State the preparation type.
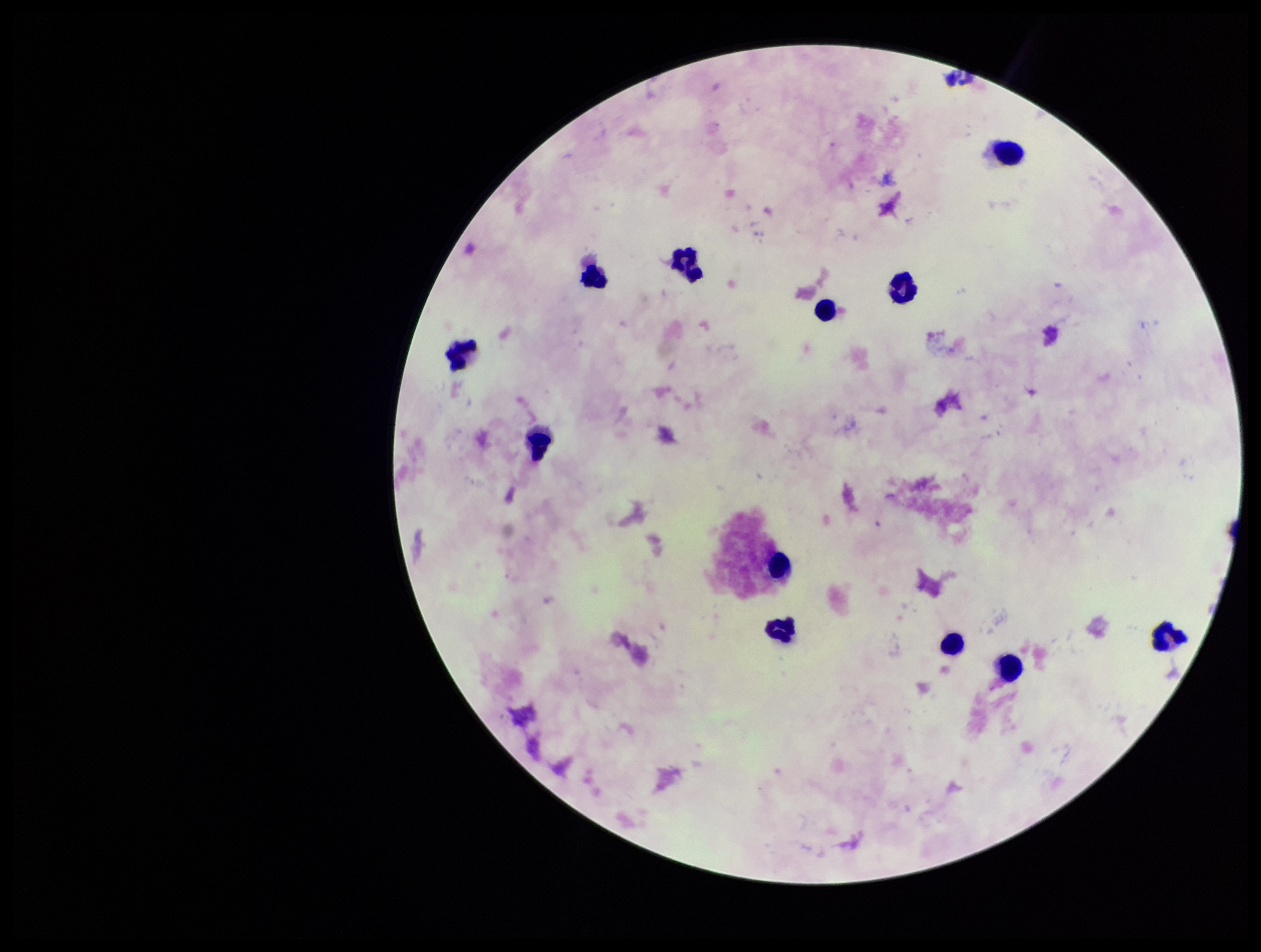

It is a thick blood smear.

Leukocyte count: 12. Stained with Giemsa. One field from this slide. Parasite count: 0. Smartphone photograph taken through the eyepiece of a microscope. Plasmodium parasites: none identified. Image is 1261×952 pixels. Patient malaria status: negative.